Classify this cell by malaria status.
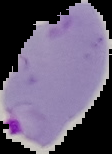

Parasitized.

From a thin blood film. Image is 112×154 pixels. The area outside the segmented cell region is set to black.